Identify the parasite.
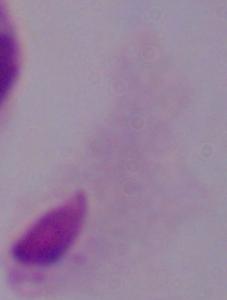
A trichomonad.

Micrograph. 1000x magnification.